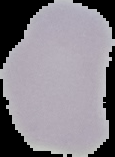

Summary:
  - Preparation: thin blood film
  - Malaria status: uninfected
  - Image type: cell region segmented out of the field of view; surrounding area masked to black
  - Image size: 115×157 pixels